Give the extent of all uninfected red blood cells.
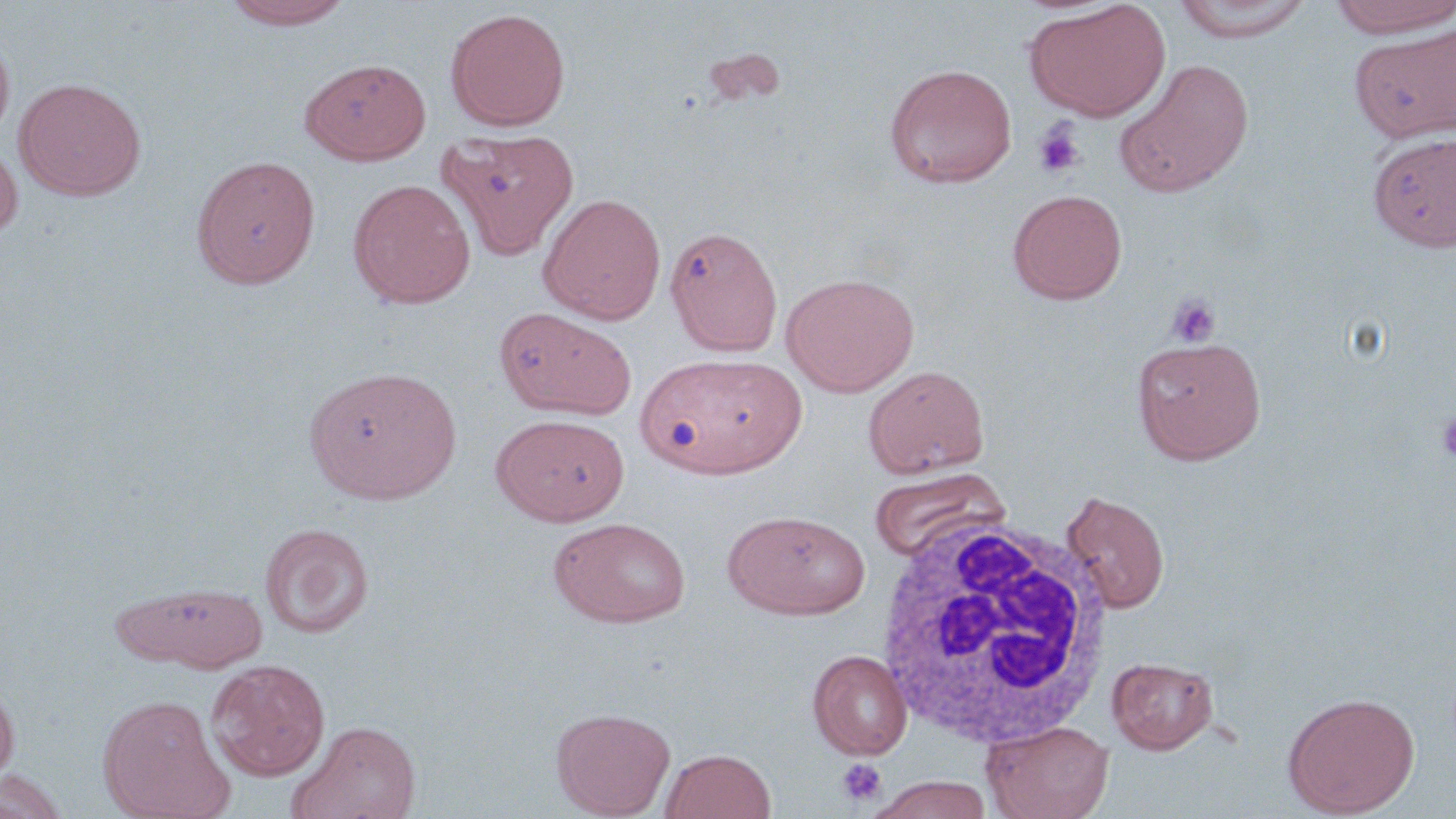
Approximate bounding boxes as named x1/y1/x2/y2 corners in pixels.
Uninfected red blood cells: (x1=221, y1=0, x2=356, y2=30), (x1=1171, y1=0, x2=1315, y2=43), (x1=1327, y1=0, x2=1456, y2=38), (x1=1025, y1=1, x2=1171, y2=122), (x1=446, y1=8, x2=570, y2=131), (x1=1351, y1=24, x2=1455, y2=143), (x1=0, y1=30, x2=15, y2=146), (x1=700, y1=47, x2=787, y2=108), (x1=299, y1=58, x2=432, y2=165), (x1=1115, y1=59, x2=1255, y2=198), (x1=884, y1=63, x2=1018, y2=187), (x1=14, y1=78, x2=146, y2=201), (x1=435, y1=127, x2=579, y2=260), (x1=1368, y1=132, x2=1456, y2=251), (x1=0, y1=140, x2=22, y2=244), (x1=191, y1=154, x2=320, y2=290), (x1=348, y1=178, x2=475, y2=309), (x1=1007, y1=189, x2=1127, y2=304), (x1=537, y1=193, x2=666, y2=325), (x1=665, y1=223, x2=783, y2=356), (x1=781, y1=273, x2=920, y2=396), (x1=495, y1=306, x2=637, y2=420), (x1=1132, y1=335, x2=1267, y2=464), (x1=638, y1=353, x2=802, y2=479), (x1=304, y1=365, x2=462, y2=504), (x1=863, y1=365, x2=989, y2=478), (x1=491, y1=413, x2=629, y2=525), (x1=869, y1=467, x2=1008, y2=564), (x1=1061, y1=489, x2=1170, y2=613), (x1=722, y1=509, x2=871, y2=620), (x1=548, y1=516, x2=691, y2=628), (x1=259, y1=522, x2=373, y2=639), (x1=112, y1=580, x2=269, y2=672), (x1=807, y1=649, x2=912, y2=760), (x1=1107, y1=656, x2=1218, y2=754), (x1=207, y1=659, x2=330, y2=781), (x1=0, y1=675, x2=19, y2=787), (x1=1282, y1=692, x2=1420, y2=818), (x1=97, y1=694, x2=233, y2=819), (x1=551, y1=706, x2=676, y2=818), (x1=287, y1=719, x2=421, y2=819), (x1=982, y1=720, x2=1114, y2=819), (x1=659, y1=748, x2=777, y2=819), (x1=0, y1=770, x2=69, y2=819), (x1=864, y1=775, x2=996, y2=818).

White blood cell locations: (x1=874, y1=512, x2=1117, y2=750). Platelet locations: (x1=1032, y1=121, x2=1086, y2=180), (x1=1165, y1=293, x2=1221, y2=347), (x1=1434, y1=412, x2=1456, y2=463), (x1=836, y1=759, x2=886, y2=808). Slide-level diagnosis: no evidence of blood parasites. Thin blood smear. Light microscopy. One field of a larger specimen. Image is 1456×819 pixels. 1000x magnification. May-Grünwald-Giemsa stain.